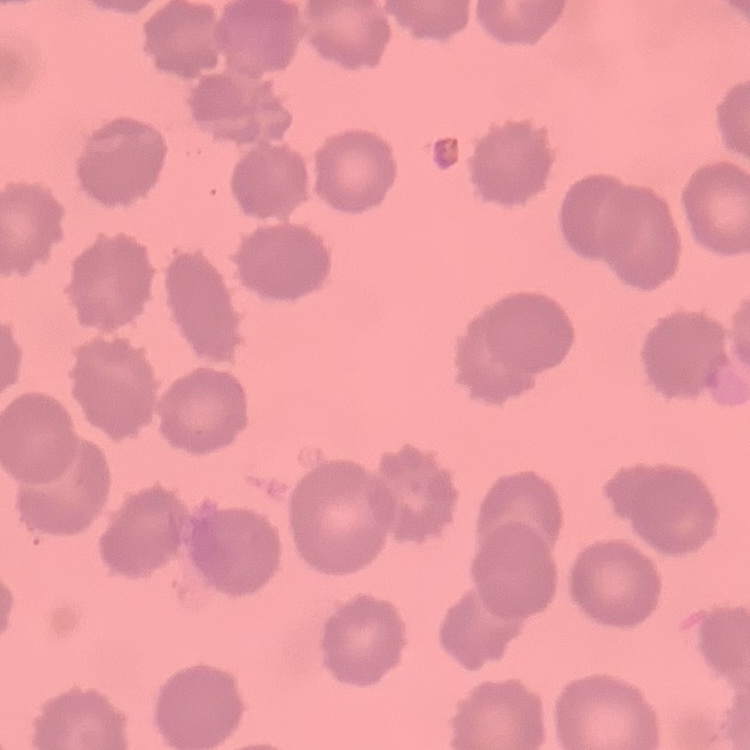
{
  "red_blood_cell_morphology": "no rouleaux formation",
  "preparation": "thin blood smear",
  "stain": "Field's or Giemsa",
  "image_type": "one tile cut from a larger photomicrograph"
}